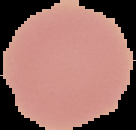

From a thin blood film. Image is 136×130 pixels. Cell region segmented out of the field of view; the surrounding area is masked to black. Malaria status: uninfected.